Report the malaria status of this cell.
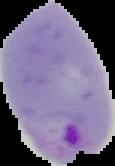

Parasitized.

{
  "preparation": "thin blood film",
  "image_size": "115×166 pixels",
  "image_type": "segmented cell region on a black background"
}